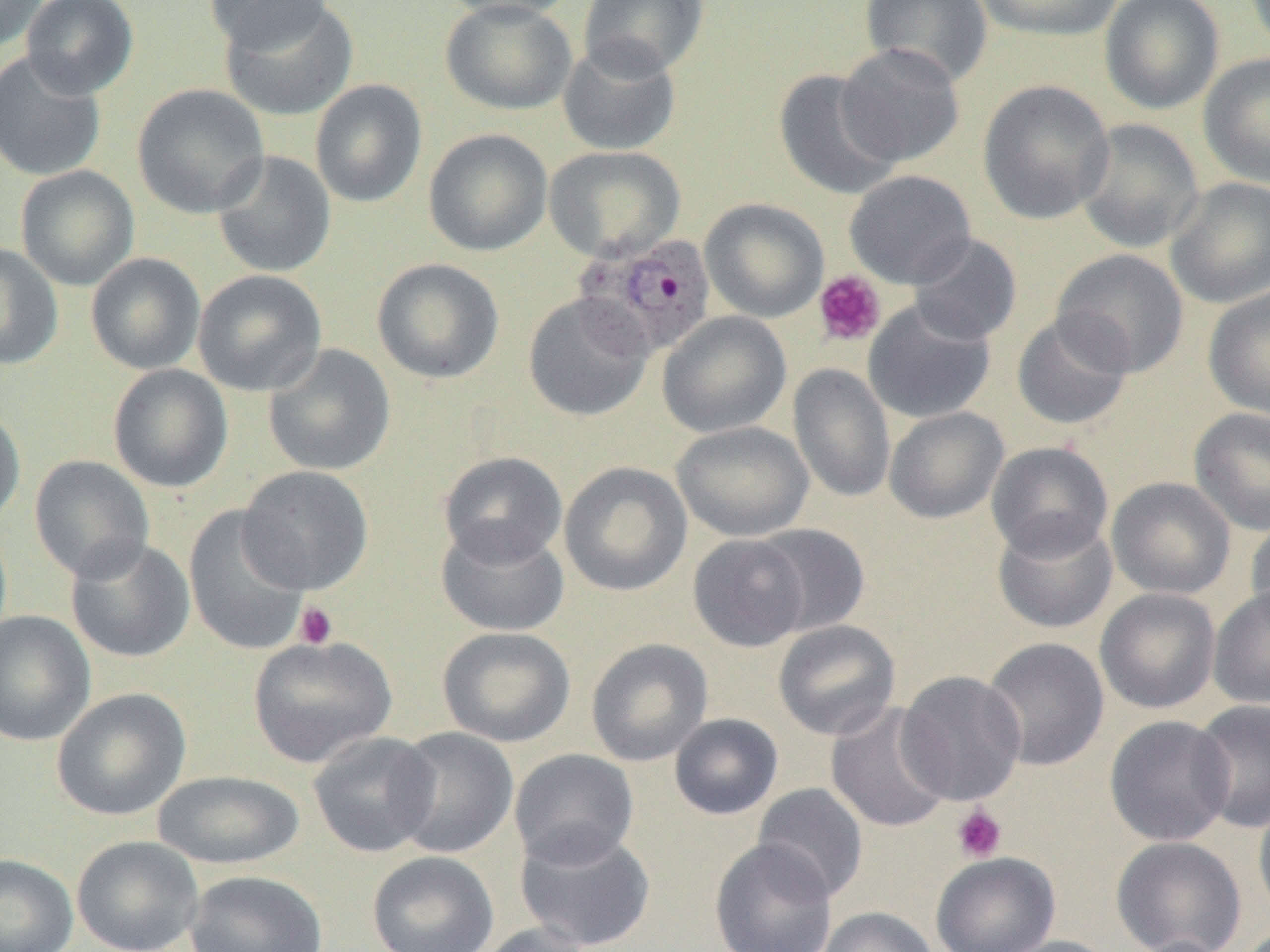 Approximate bounding boxes as [x1, y1, x2, y2] in pixels. Uninfected red blood cell locations: [0, 0, 47, 53], [20, 0, 140, 99], [204, 0, 333, 50], [434, 0, 582, 22], [579, 0, 710, 79], [860, 0, 993, 87], [972, 0, 1125, 41], [1099, 0, 1225, 115], [217, 1, 359, 121], [440, 1, 578, 116], [557, 39, 681, 156], [835, 43, 965, 167], [0, 49, 107, 182], [1198, 52, 1270, 188], [773, 69, 903, 201], [309, 79, 428, 208], [977, 80, 1115, 224], [132, 84, 270, 219], [1074, 118, 1204, 254], [422, 128, 552, 256], [543, 145, 686, 263], [211, 150, 336, 278], [15, 165, 139, 290], [844, 170, 976, 288], [1165, 177, 1270, 308], [700, 198, 829, 323], [907, 233, 1022, 346], [0, 241, 63, 370], [1052, 248, 1189, 378], [85, 252, 206, 375], [372, 257, 505, 384], [193, 269, 327, 397], [1202, 286, 1270, 420], [523, 292, 653, 422], [863, 299, 996, 424], [657, 311, 791, 438], [1012, 312, 1134, 431], [263, 344, 396, 476], [788, 363, 896, 504], [107, 364, 234, 493], [0, 404, 26, 530], [884, 407, 1009, 524], [1189, 407, 1270, 536], [672, 421, 813, 541], [986, 440, 1114, 560], [438, 451, 568, 567], [29, 455, 154, 582], [559, 461, 693, 597], [238, 465, 374, 594], [1106, 476, 1236, 599], [183, 505, 310, 657], [991, 514, 1118, 633], [1245, 516, 1270, 632], [436, 521, 569, 636], [753, 524, 869, 636], [687, 533, 811, 651], [65, 537, 195, 663], [1208, 586, 1270, 709], [1094, 588, 1221, 714], [0, 611, 95, 746], [772, 619, 901, 740], [437, 626, 576, 747], [247, 636, 397, 767], [981, 637, 1110, 771], [586, 638, 713, 767], [896, 670, 1027, 806], [51, 687, 191, 821], [1191, 699, 1270, 833], [826, 703, 953, 834], [668, 713, 784, 820], [1104, 714, 1237, 847], [390, 727, 518, 858], [308, 731, 441, 857], [510, 748, 639, 868], [152, 770, 304, 869], [752, 782, 868, 902], [1253, 794, 1270, 926], [514, 826, 656, 951], [71, 835, 203, 952], [1110, 836, 1247, 952], [709, 838, 838, 952], [367, 850, 499, 952], [931, 852, 1060, 952], [0, 853, 79, 952], [184, 869, 328, 952], [817, 906, 939, 952], [473, 922, 597, 952], [991, 935, 1122, 952], [1124, 935, 1235, 952]. Plasmodium ovale-infected red blood cell locations: [572, 232, 718, 359]. Platelet locations: [813, 269, 886, 347], [294, 601, 338, 649], [952, 805, 1007, 862]. Slide-level diagnosis: Plasmodium ovale. Thin blood smear. 1000x magnification. Single field of view. Image is 1270×952 pixels. Optical microscopy.